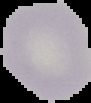 Segmented cell region on a black background. Image is 91×103 pixels. From a thin blood film. Result: negative for malaria parasites.